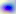
Summary:
  - Magnification: 400x
  - Identification: Toxoplasma gondii
  - Modality: photomicrograph